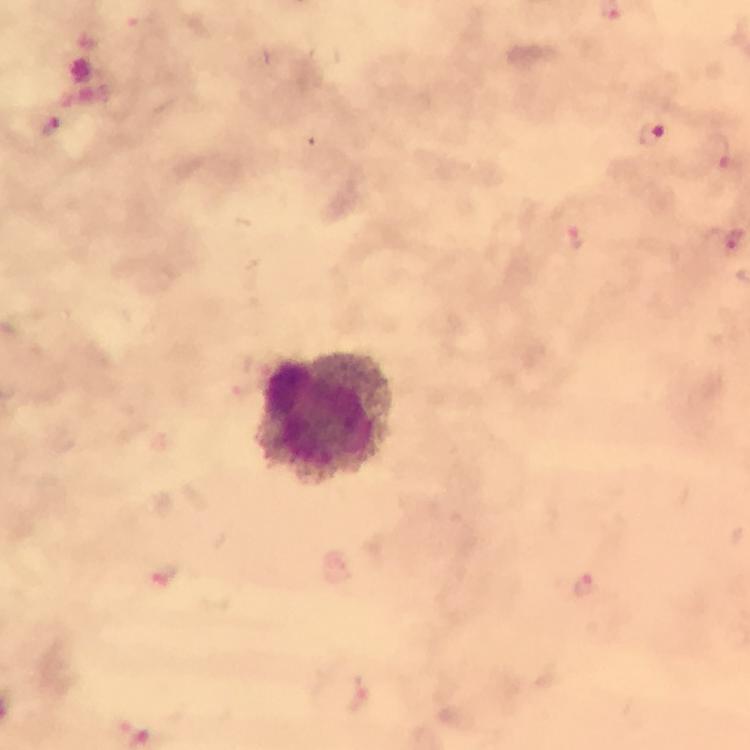
Approximate centers as [x, y] in pixels.
Summary:
  - Plasmodium parasite locations: [53, 127], [653, 135], [721, 152], [727, 239], [571, 240], [166, 575], [586, 585]
  - Leukocyte locations: [325, 416]
  - Capture: smartphone mounted on the microscope
  - Magnification: 100x
  - Preparation: thick smear
  - Stain: Giemsa
  - Image size: 750×750 pixels
  - Context: from a malaria diagnostic workup
  - Cropped from: one field of view
  - Immersion oil: applied